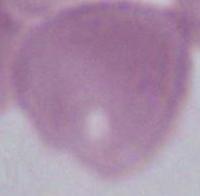
A red blood cell is shown. Photomicrograph. Captured at 1000x magnification.